Assess the morphology of the red blood cells.
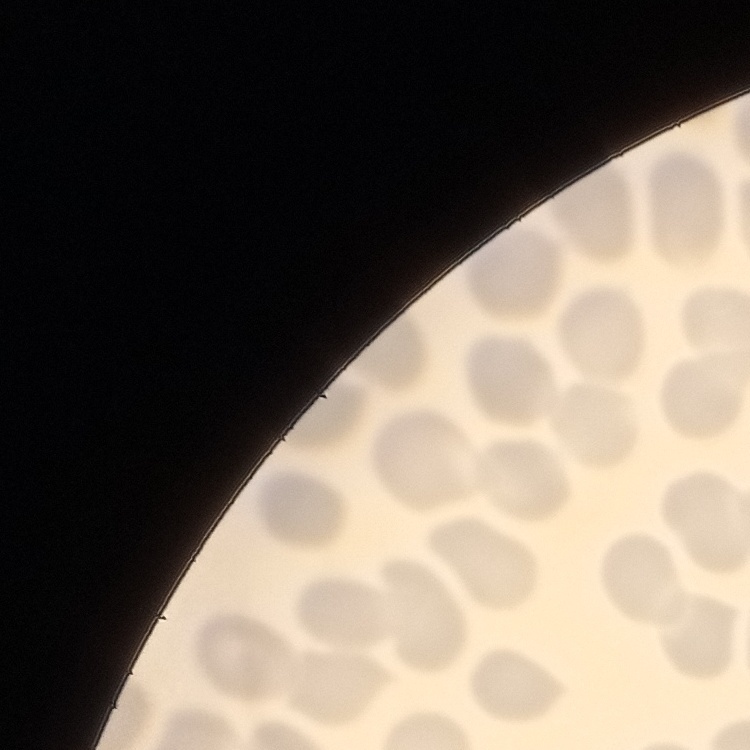

No rouleaux formation.

Summary:
  - Image type: one tile cut from a larger photomicrograph
  - Stain: Field's or Giemsa
  - Preparation: thin peripheral smear